Assess this cell for malaria.
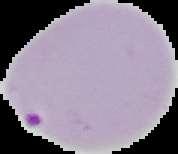
Parasitized.

Summary:
  - Image size: 178×154 pixels
  - Preparation: thin blood film
  - Image type: segmented cell region with the area outside set to black